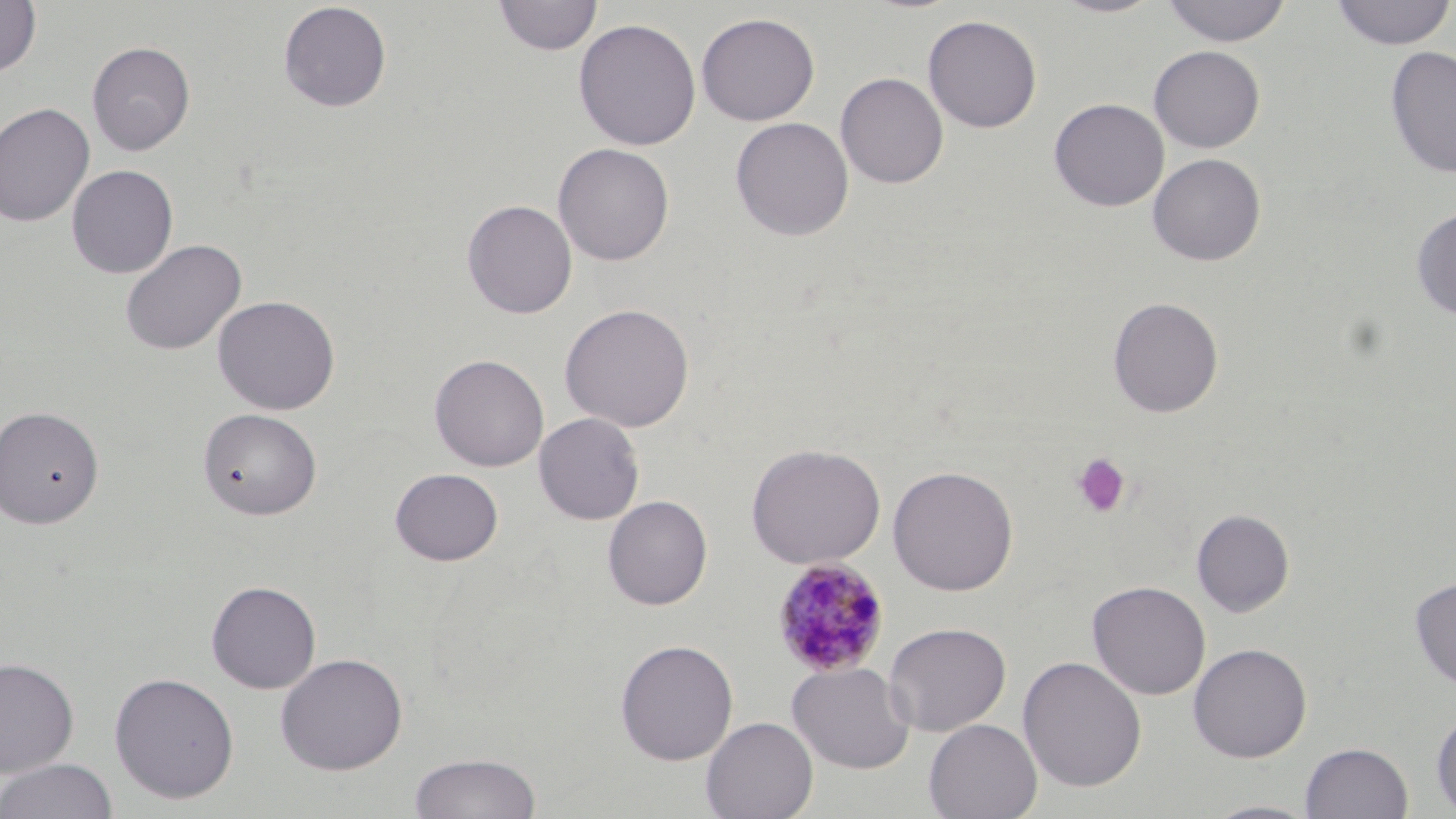

slide-level diagnosis = Plasmodium malariae
preparation = thin blood film
uninfected red blood cell locations = approximate bounding boxes as (x1,y1)-(x2,y2) corner pairs in pixels: (493,0)-(602,56), (1051,0)-(1164,18), (1160,0)-(1293,47), (1330,0)-(1455,50), (0,1)-(41,77), (277,1)-(392,113), (696,12)-(820,126), (922,15)-(1042,133), (573,18)-(701,151), (87,41)-(195,156), (1149,45)-(1265,153), (1385,45)-(1456,180), (835,72)-(949,189), (1048,98)-(1169,212), (0,102)-(95,228), (730,117)-(854,241), (553,143)-(675,266), (1148,153)-(1266,266), (67,165)-(178,279), (462,199)-(577,319), (1411,206)-(1456,321), (120,239)-(247,357), (212,295)-(340,415), (1107,296)-(1223,418), (559,303)-(695,433), (429,354)-(549,472), (0,405)-(104,528), (198,408)-(322,520), (533,412)-(645,525), (746,442)-(886,569), (887,464)-(1019,596), (390,467)-(504,566), (602,495)-(713,610), (1192,508)-(1295,617), (1409,576)-(1456,690), (206,580)-(321,693), (1087,580)-(1211,700), (884,621)-(1011,736), (615,639)-(739,765), (1188,643)-(1312,762), (275,652)-(407,774), (1018,655)-(1147,793), (0,657)-(79,776), (787,661)-(916,774), (109,671)-(240,803), (1430,708)-(1456,815), (700,716)-(818,819), (924,719)-(1042,819), (1300,742)-(1414,819), (408,752)-(542,819), (0,758)-(120,819), (1202,799)-(1322,819)
modality = optical microscopy
magnification = 1000x
field of view = single
Plasmodium malariae-infected red blood cell locations = approximate bounding boxes as (x1,y1)-(x2,y2) corner pairs in pixels: (771,557)-(891,677)
image size = 1456×819 pixels
platelet locations = approximate bounding boxes as (x1,y1)-(x2,y2) corner pairs in pixels: (1071,452)-(1132,518)
stain = May-Grünwald-Giemsa